State the preparation type.
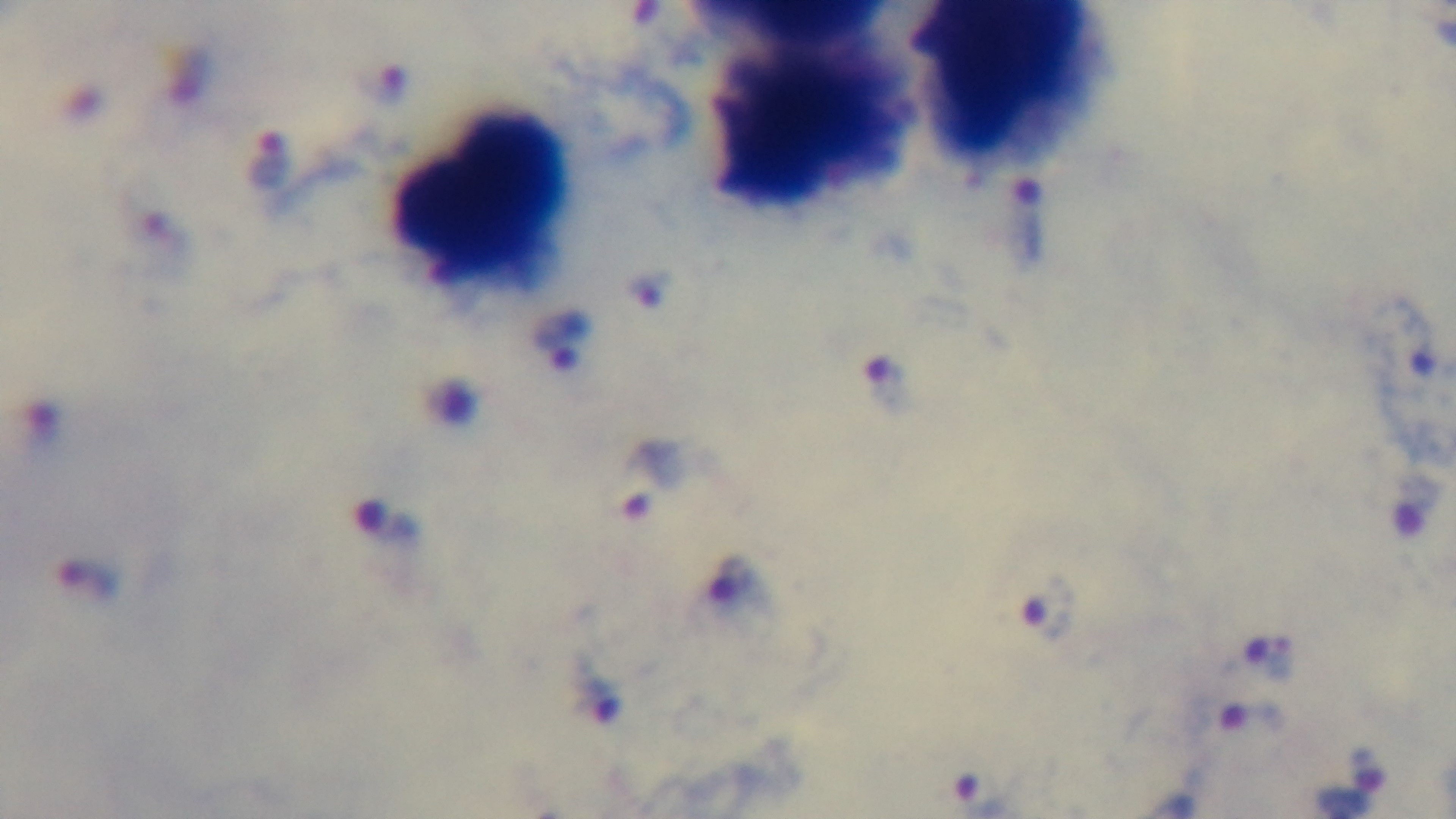
Thick.

Malaria status: infected. Single field of view. Light microscopy. 100x oil-immersion objective. Captured with a mounted 4K digital camera. Giemsa stain.